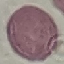

Summary:
  - Result: no malaria parasites detected
  - Preparation: thin blood film
  - Image type: cell patch, automatically extracted from a larger field of view and resized to 64 × 64 pixels
  - Capture: smartphone through the microscope eyepiece
  - Stain: Giemsa